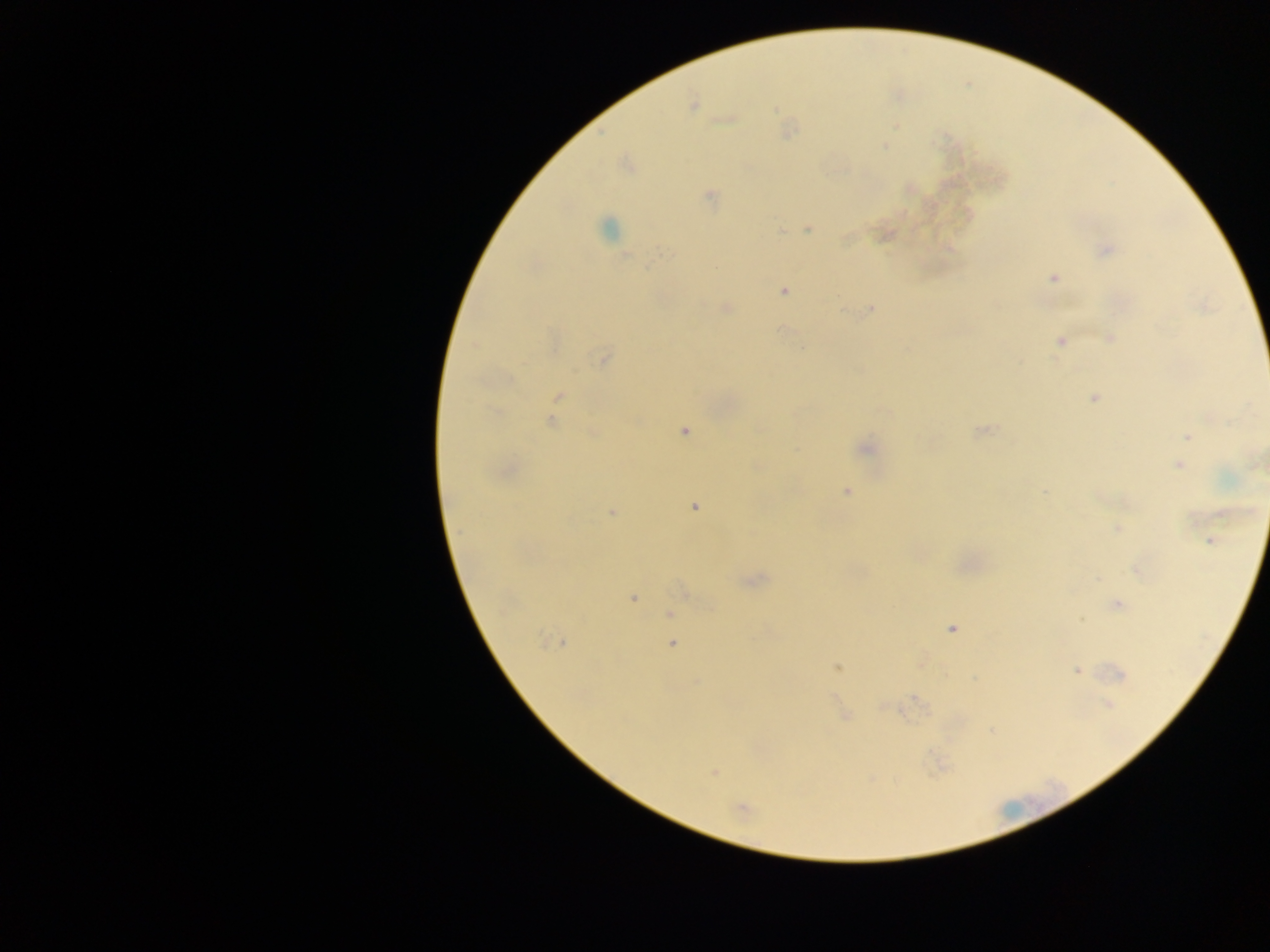

malaria parasite locations = approximate centers as (x, y) in pixels: (693, 103), (726, 120), (884, 146), (710, 196), (607, 228), (807, 229), (780, 230), (846, 239), (1105, 250), (663, 254), (627, 257), (1053, 278), (783, 292), (726, 309), (871, 309), (843, 311), (1109, 338), (1060, 341), (603, 358), (558, 396), (1094, 397), (551, 422), (980, 430), (685, 431), (1187, 436), (867, 449), (1178, 465), (847, 492), (1043, 492), (694, 507), (612, 512), (1116, 529), (1210, 541), (1138, 572), (1097, 579), (755, 580), (684, 591), (633, 597), (1118, 605), (671, 614), (1081, 620), (952, 628), (558, 642), (672, 644), (838, 667), (1076, 670), (1119, 675), (695, 682), (916, 699), (1108, 705), (882, 707), (845, 716), (714, 772), (741, 809)
preparation = thick blood smear
capture = mobile-phone photograph through a microscope
image size = 1270×952 pixels
field of view = single
country = Ghana